Outline each blood parasite and name the species.
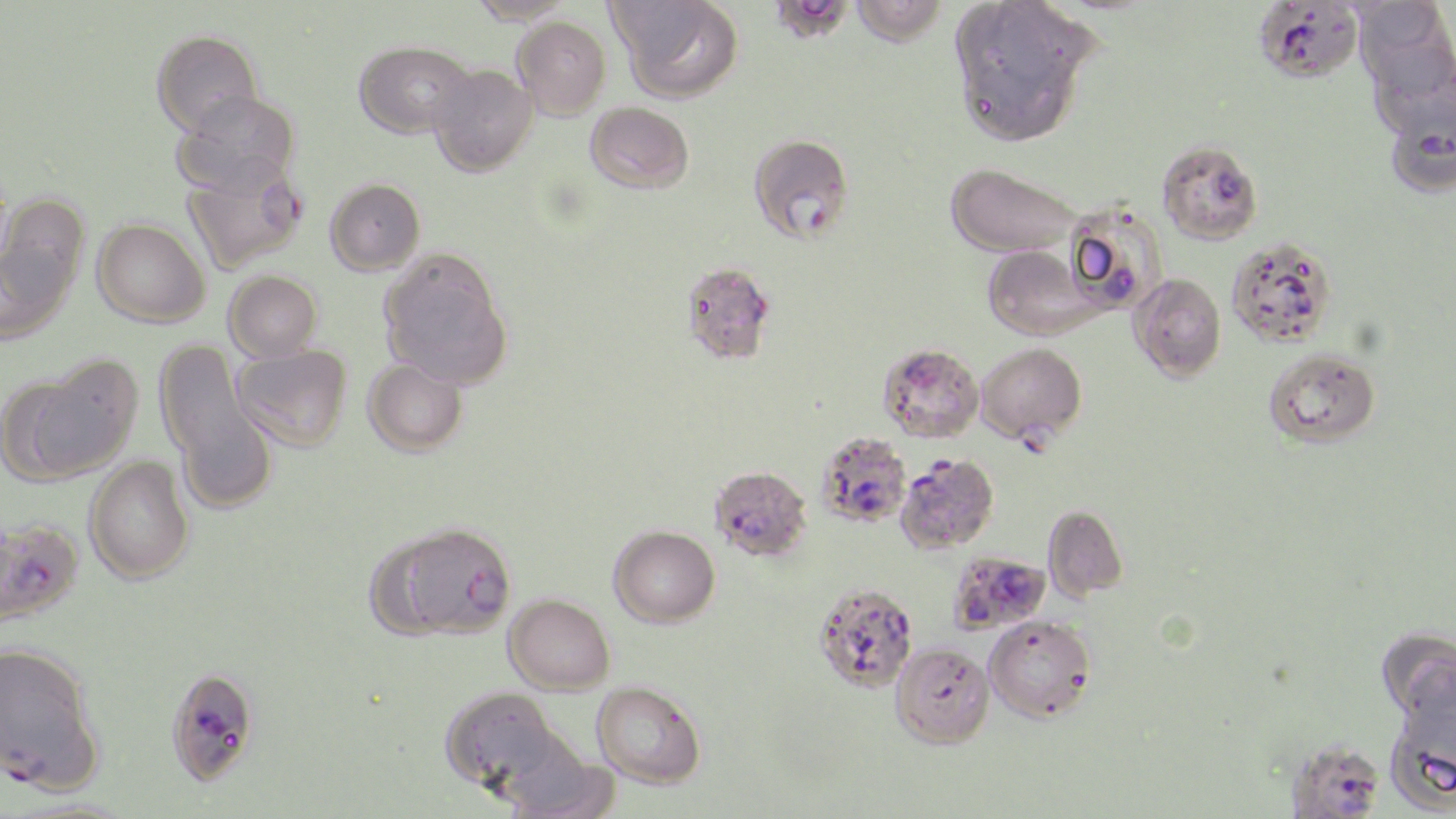
Approximate bounding boxes as [x1, y1, x2, y2] in pixels.
Plasmodium falciparum-infected red blood cells: [777, 0, 855, 48], [1252, 0, 1363, 84], [1387, 103, 1456, 203], [748, 133, 854, 243], [183, 160, 306, 274], [1061, 201, 1166, 313], [680, 261, 776, 365], [976, 342, 1087, 464], [878, 343, 984, 442], [816, 431, 912, 527], [895, 453, 999, 554], [709, 466, 812, 561], [0, 518, 84, 625], [378, 522, 518, 640], [951, 553, 1054, 637], [812, 583, 918, 692], [0, 640, 105, 793], [164, 665, 261, 787], [1285, 740, 1386, 818].
No Plasmodium ovale, Plasmodium malariae, Plasmodium vivax, Babesia divergens, or Trypanosoma brucei observed.

slide_level_diagnosis: Plasmodium falciparum
field_of_view: one of a larger specimen
image_size: 1456×819 pixels
uninfected_red_blood_cell_locations: 'approximate bounding boxes as [x1, y1, x2, y2] in pixels: [464, 0, 580, 24], [611, 0, 743, 103], [850, 0, 948, 46], [947, 1, 1095, 145], [1353, 1, 1455, 96], [511, 16, 610, 119], [151, 30, 263, 137], [354, 40, 475, 138], [1369, 53, 1456, 146], [427, 65, 537, 177], [173, 90, 301, 196], [585, 102, 694, 194], [1156, 140, 1263, 245], [945, 162, 1082, 258], [325, 178, 425, 275], [2, 193, 90, 298], [92, 218, 210, 327], [1226, 236, 1338, 348], [0, 238, 76, 345], [981, 245, 1102, 341], [378, 248, 514, 389], [224, 270, 323, 362], [1129, 273, 1226, 382], [156, 344, 274, 506], [232, 344, 353, 451], [1263, 348, 1381, 449], [363, 358, 468, 457], [8, 362, 138, 482], [84, 457, 194, 585], [1042, 504, 1129, 602], [609, 525, 720, 627], [504, 593, 615, 694], [984, 614, 1096, 722], [1375, 627, 1456, 724], [891, 643, 995, 749], [592, 681, 706, 788], [441, 686, 569, 797], [1384, 686, 1456, 812], [3, 798, 145, 819]'
magnification: 1000x
stain: May-Grünwald-Giemsa
preparation: thin blood film
modality: optical microscopy